Locate platelets.
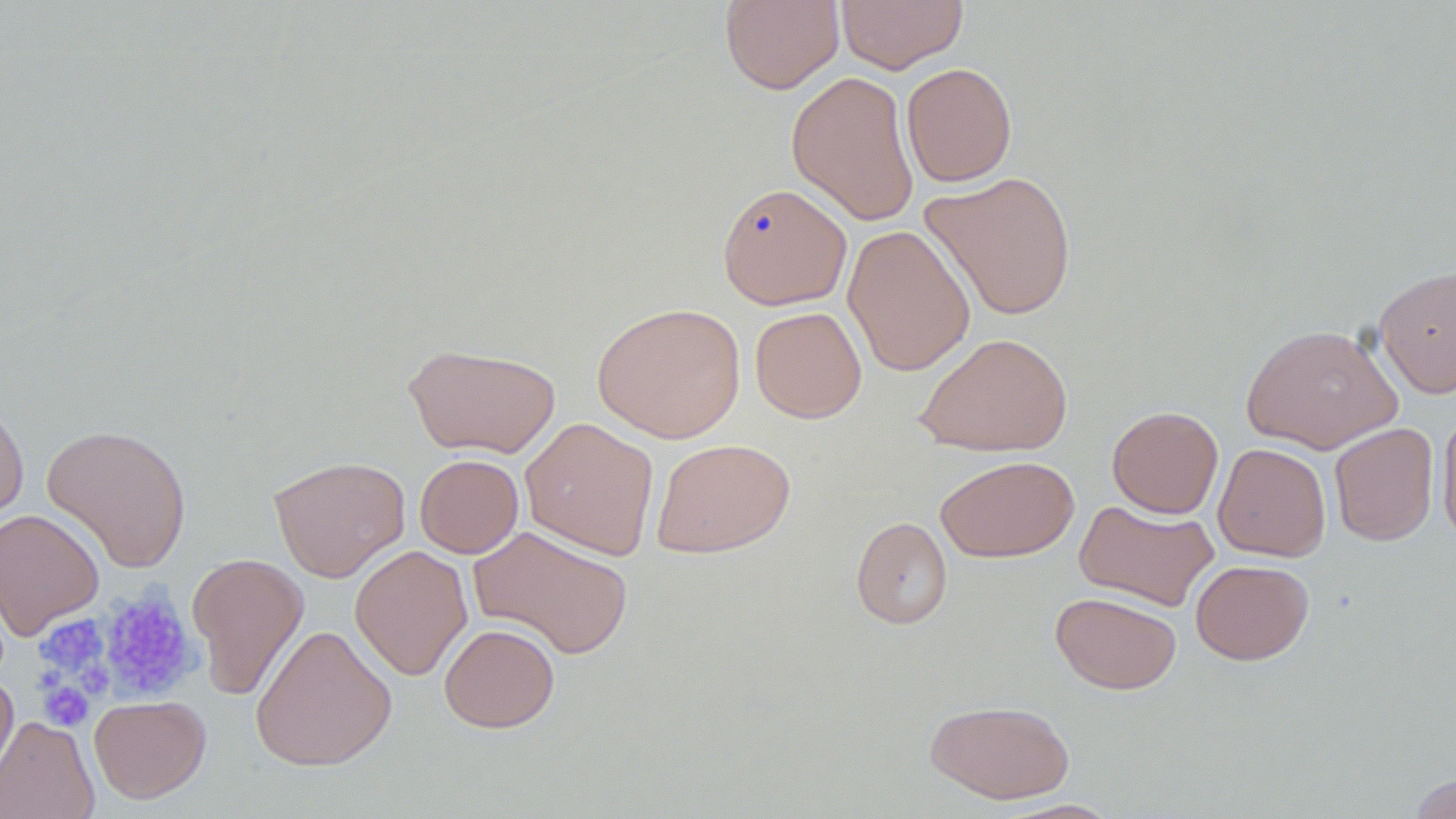

Approximate bounding boxes as (x1, y1, x2, y2) in pixels.
Platelets: (97, 588, 201, 705), (34, 614, 111, 679), (38, 679, 94, 731).

slide-level diagnosis = no evidence of blood parasites
stain = May-Grünwald-Giemsa
field of view = single
image size = 1456×819 pixels
uninfected red blood cell locations = approximate bounding boxes as (x1, y1, x2, y2) in pixels: (719, 0, 844, 94), (835, 0, 968, 73), (901, 62, 1017, 187), (786, 70, 920, 226), (919, 171, 1078, 321), (717, 182, 853, 310), (842, 223, 976, 377), (1373, 265, 1456, 399), (592, 302, 747, 444), (750, 306, 867, 423), (1241, 323, 1402, 454), (914, 331, 1073, 458), (402, 342, 561, 458), (0, 392, 30, 522), (1107, 405, 1224, 519), (1437, 409, 1456, 548), (519, 417, 659, 560), (1329, 422, 1440, 546), (41, 423, 192, 573), (651, 438, 795, 559), (1213, 443, 1331, 562), (415, 454, 524, 558), (268, 455, 410, 582), (935, 455, 1079, 562), (1074, 499, 1219, 611), (0, 508, 105, 640), (851, 516, 953, 629), (469, 525, 634, 660), (350, 544, 472, 681), (187, 552, 309, 701), (1190, 559, 1314, 665), (1050, 591, 1182, 694), (250, 623, 397, 771), (439, 623, 560, 733), (0, 670, 19, 790), (89, 694, 211, 803), (925, 698, 1075, 804), (0, 715, 99, 819), (1409, 772, 1456, 818), (999, 799, 1123, 818)
preparation = thin blood film
magnification = 1000x
modality = light microscopy